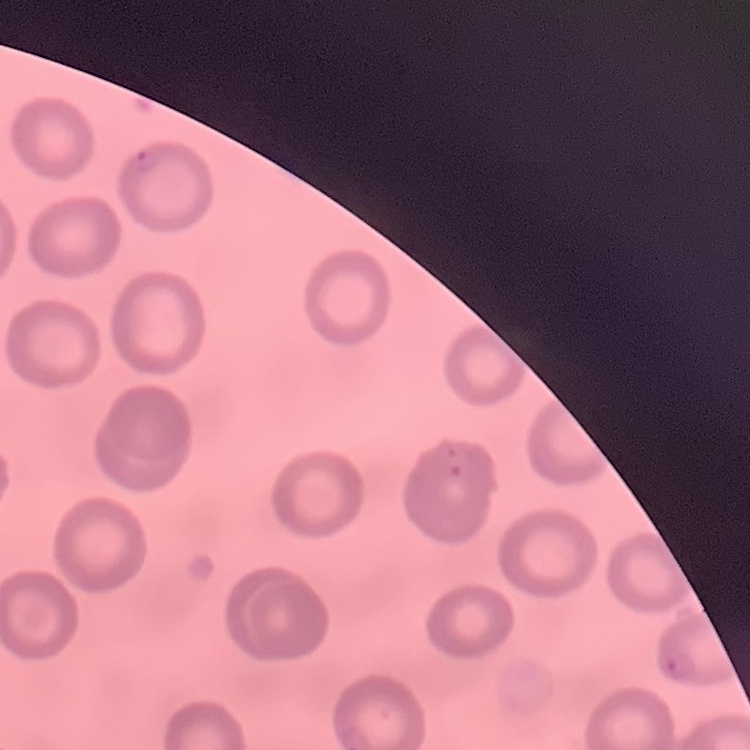

erythrocyte_morphology: no rouleaux formation
stain: Field's or Giemsa
image_type: one tile cut from a larger photomicrograph
preparation: thin peripheral smear